Identify the cell.
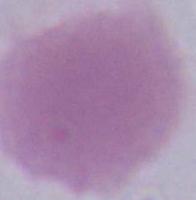

An erythrocyte.

Photomicrograph. Captured at 1000x magnification.